Report the malaria status of this cell.
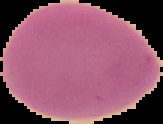

It is uninfected.

Summary:
  - Image size: 163×124 pixels
  - Preparation: thin blood film
  - Image type: segmented cell region on a black background